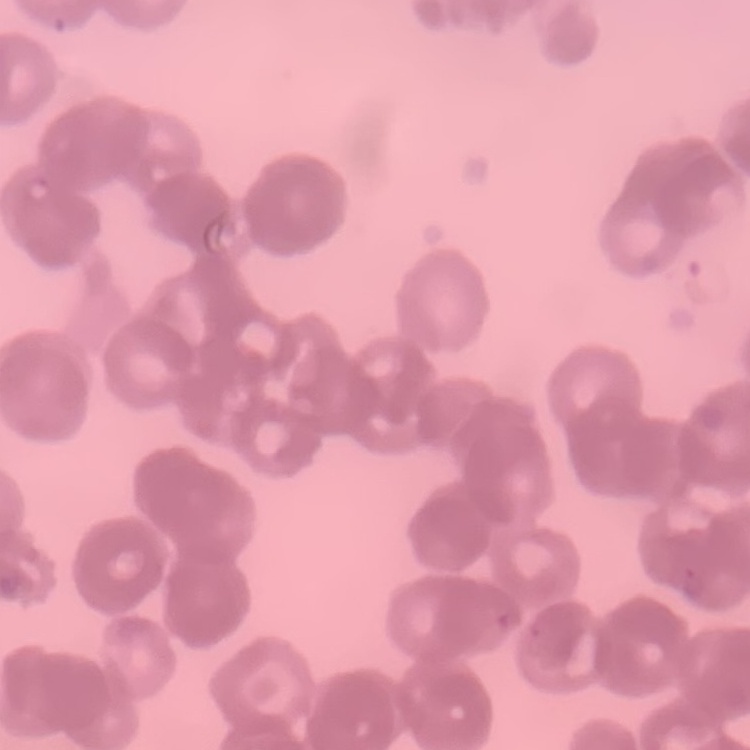

Summary:
  - Erythrocyte morphology: rouleaux formation
  - Preparation: thin blood film
  - Image type: one tile cut from a larger photomicrograph
  - Stain: Field's or Giemsa